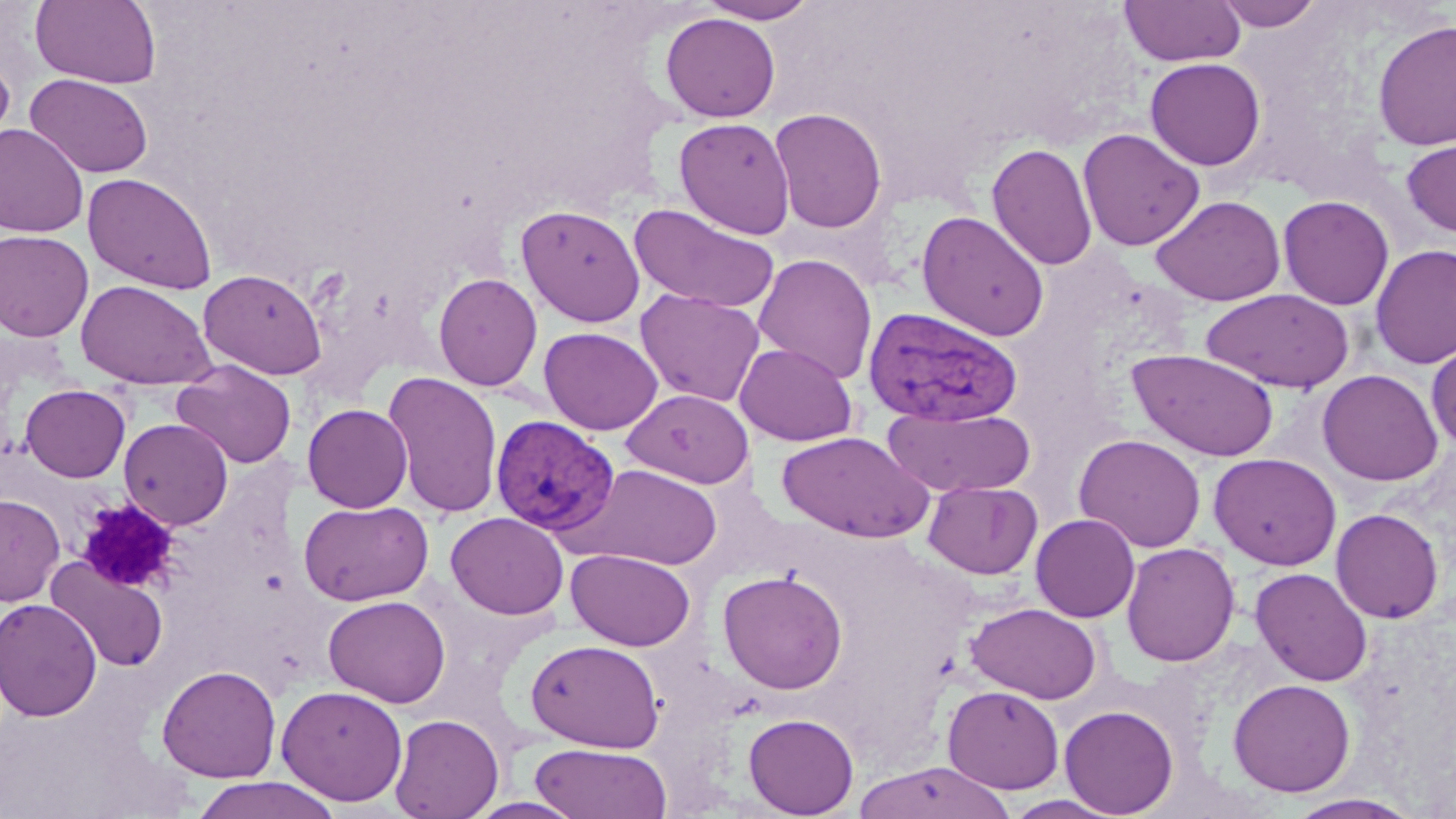
Summary:
  - Coordinate format: approximate bounding boxes as named x1/y1/x2/y2 corners in pixels
  - Platelet locations: (x1=76, y1=499, x2=182, y2=593)
  - Uninfected red blood cell locations: (x1=31, y1=0, x2=161, y2=89), (x1=698, y1=0, x2=820, y2=24), (x1=1120, y1=0, x2=1245, y2=67), (x1=1215, y1=0, x2=1325, y2=31), (x1=660, y1=12, x2=780, y2=122), (x1=1372, y1=19, x2=1456, y2=152), (x1=0, y1=52, x2=15, y2=156), (x1=1145, y1=57, x2=1266, y2=170), (x1=26, y1=73, x2=153, y2=178), (x1=769, y1=107, x2=887, y2=234), (x1=674, y1=117, x2=795, y2=239), (x1=0, y1=125, x2=89, y2=237), (x1=1078, y1=128, x2=1205, y2=251), (x1=1401, y1=136, x2=1456, y2=238), (x1=987, y1=142, x2=1098, y2=271), (x1=82, y1=172, x2=218, y2=294), (x1=1151, y1=195, x2=1286, y2=306), (x1=1278, y1=195, x2=1394, y2=310), (x1=627, y1=203, x2=780, y2=314), (x1=516, y1=204, x2=646, y2=327), (x1=916, y1=211, x2=1050, y2=342), (x1=0, y1=230, x2=94, y2=341), (x1=1371, y1=244, x2=1456, y2=369), (x1=753, y1=254, x2=877, y2=385), (x1=199, y1=268, x2=327, y2=379), (x1=432, y1=272, x2=543, y2=391), (x1=76, y1=279, x2=214, y2=389), (x1=635, y1=288, x2=765, y2=407), (x1=1201, y1=288, x2=1354, y2=393), (x1=538, y1=326, x2=663, y2=435), (x1=1427, y1=338, x2=1456, y2=451), (x1=735, y1=343, x2=857, y2=446), (x1=1127, y1=349, x2=1280, y2=462), (x1=171, y1=360, x2=297, y2=469), (x1=1317, y1=369, x2=1443, y2=486), (x1=383, y1=372, x2=504, y2=519), (x1=20, y1=384, x2=130, y2=482), (x1=622, y1=388, x2=754, y2=488), (x1=302, y1=403, x2=413, y2=512), (x1=883, y1=406, x2=1036, y2=498), (x1=119, y1=418, x2=233, y2=529), (x1=776, y1=431, x2=933, y2=543), (x1=1073, y1=433, x2=1206, y2=553), (x1=1208, y1=453, x2=1342, y2=571), (x1=567, y1=464, x2=724, y2=570), (x1=922, y1=480, x2=1042, y2=579), (x1=0, y1=494, x2=64, y2=605), (x1=297, y1=499, x2=434, y2=606), (x1=1331, y1=508, x2=1444, y2=623), (x1=445, y1=512, x2=569, y2=620), (x1=1031, y1=513, x2=1140, y2=622), (x1=1121, y1=541, x2=1240, y2=667), (x1=566, y1=549, x2=695, y2=651), (x1=46, y1=557, x2=168, y2=672), (x1=1250, y1=567, x2=1373, y2=686), (x1=717, y1=569, x2=848, y2=694), (x1=323, y1=595, x2=451, y2=707), (x1=0, y1=598, x2=102, y2=722), (x1=966, y1=602, x2=1102, y2=704), (x1=527, y1=639, x2=664, y2=752), (x1=157, y1=664, x2=281, y2=783), (x1=1228, y1=678, x2=1356, y2=796), (x1=276, y1=685, x2=408, y2=805), (x1=942, y1=685, x2=1064, y2=793), (x1=1059, y1=704, x2=1179, y2=817), (x1=743, y1=713, x2=859, y2=818), (x1=390, y1=714, x2=503, y2=819), (x1=529, y1=743, x2=671, y2=818), (x1=852, y1=761, x2=1016, y2=819), (x1=188, y1=776, x2=344, y2=819), (x1=1282, y1=792, x2=1425, y2=818), (x1=1001, y1=794, x2=1125, y2=818), (x1=462, y1=796, x2=589, y2=818)
  - Plasmodium vivax-infected red blood cell locations: (x1=862, y1=306, x2=1023, y2=428), (x1=490, y1=414, x2=620, y2=537)
  - Slide-level diagnosis: Plasmodium vivax
  - Modality: light microscopy
  - Image size: 1456×819 pixels
  - Field of view: single
  - Stain: May-Grünwald-Giemsa
  - Preparation: thin blood film
  - Magnification: 1000x